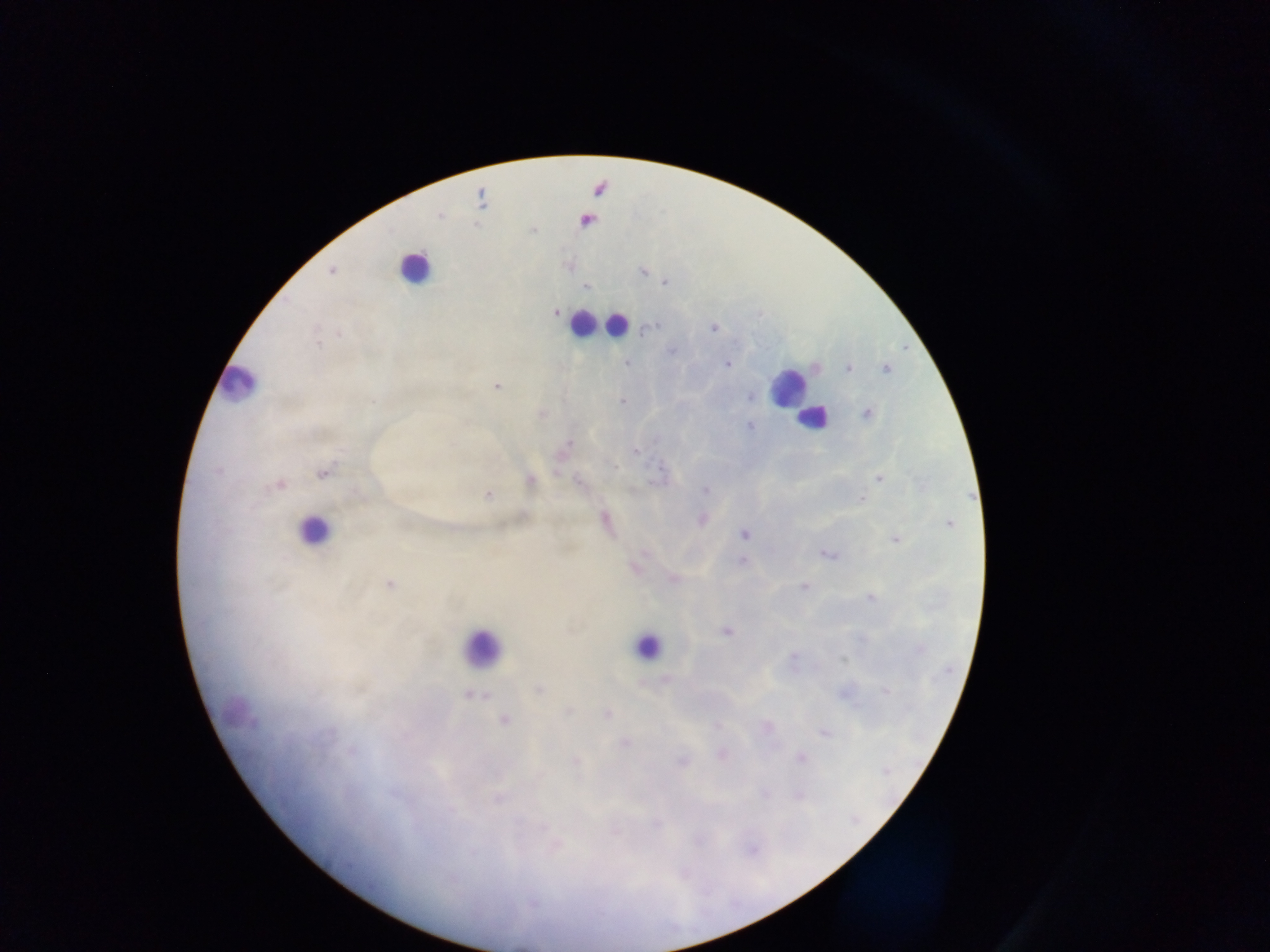 Approximate centers as (x, y) in pixels. Leukocyte locations: (599, 189), (588, 222), (415, 267), (583, 322), (616, 325), (237, 382), (787, 387), (811, 418), (313, 530), (646, 645), (481, 648). Plasmodium parasite locations: (533, 230), (332, 271), (643, 272), (664, 282), (585, 287), (555, 313), (713, 328), (649, 329), (339, 333), (318, 345), (672, 352), (627, 363), (727, 364), (848, 368), (885, 368), (495, 386), (750, 396), (372, 401), (622, 401), (867, 413), (541, 414), (751, 426), (567, 444), (635, 451), (615, 467), (322, 472), (659, 474), (879, 478), (530, 480), (578, 482), (280, 485), (704, 490), (488, 494), (861, 498), (702, 519), (606, 520), (949, 524), (743, 534), (895, 540), (828, 554), (741, 562), (636, 567), (673, 579), (390, 584), (804, 587), (869, 598), (726, 632), (919, 650), (793, 658), (843, 660), (664, 679), (538, 689), (885, 692), (468, 695), (568, 712), (607, 713), (504, 721), (716, 727), (766, 727), (824, 732), (623, 744), (721, 754), (800, 757), (576, 760), (682, 761), (886, 771), (765, 793), (615, 831). Collected in Ghana. One field of view. Image is 1270×952 pixels. Photographed through a microscope with a mobile-phone camera. Thick blood smear.